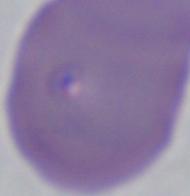 1000x magnification. A Babesia parasite is shown. Photomicrograph.